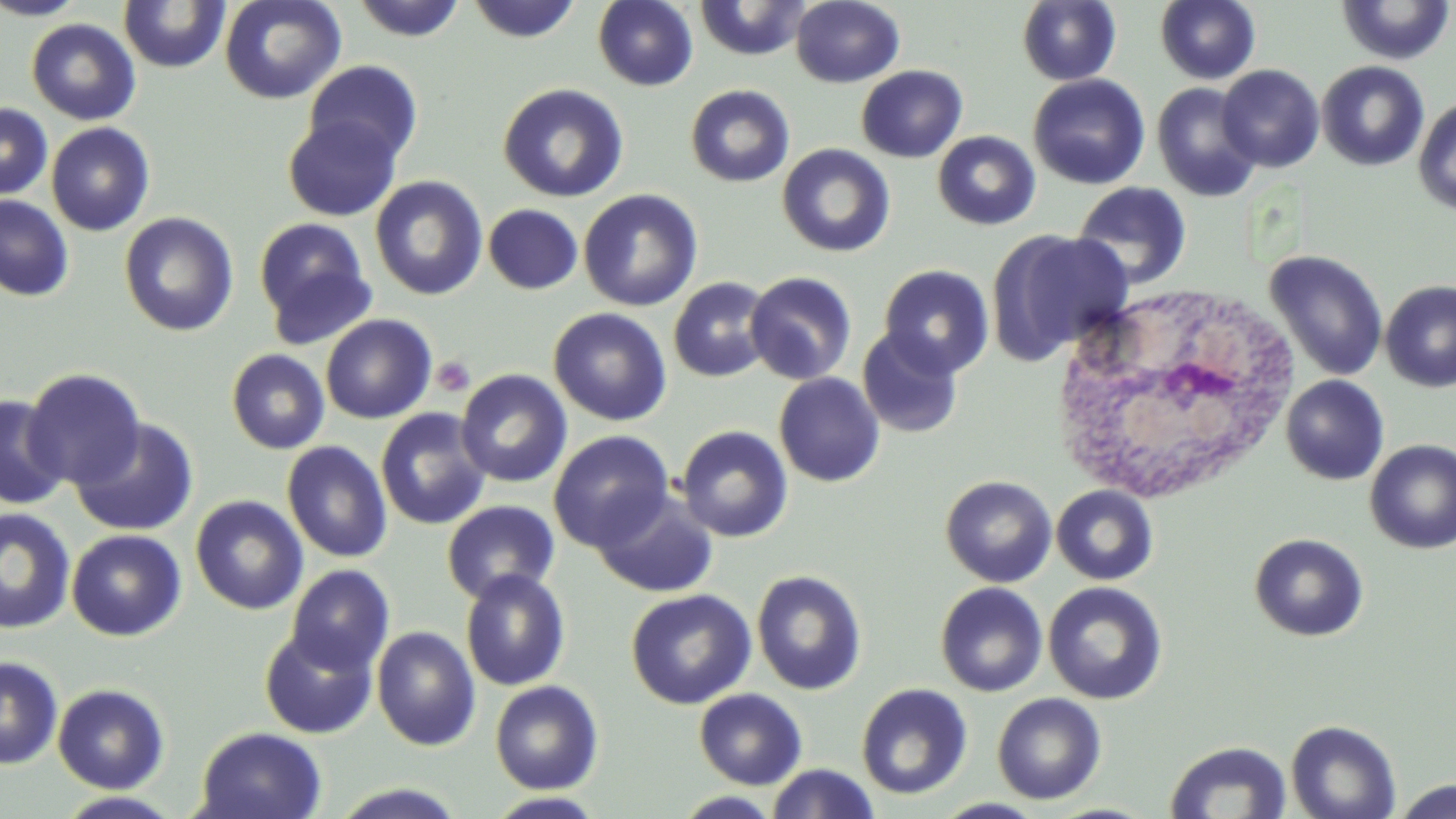
Summary:
  - Coordinate format: approximate bounding boxes as [x1, y1, x2, y2] in pixels
  - Platelet locations: [432, 355, 476, 397]
  - White blood cell locations: [1054, 290, 1305, 502]
  - Uninfected red blood cell locations: [0, 0, 91, 20], [218, 0, 346, 104], [349, 0, 469, 42], [465, 0, 583, 43], [692, 0, 814, 61], [791, 0, 905, 88], [1154, 0, 1261, 84], [1335, 0, 1456, 65], [118, 1, 230, 73], [592, 1, 698, 91], [1017, 1, 1121, 86], [26, 19, 141, 125], [303, 59, 423, 168], [1316, 61, 1429, 171], [1216, 64, 1325, 172], [856, 65, 968, 163], [1028, 74, 1150, 190], [498, 83, 629, 203], [1151, 83, 1262, 202], [685, 84, 795, 187], [1413, 97, 1456, 214], [0, 102, 52, 200], [283, 114, 402, 221], [45, 122, 155, 236], [932, 131, 1041, 230], [777, 143, 895, 257], [369, 176, 488, 301], [1071, 182, 1192, 290], [577, 189, 703, 311], [0, 194, 74, 302], [483, 204, 583, 294], [119, 212, 238, 336], [254, 217, 377, 342], [987, 229, 1133, 363], [1265, 250, 1388, 381], [878, 264, 994, 378], [744, 271, 858, 385], [668, 276, 774, 382], [1380, 280, 1456, 392], [548, 308, 672, 426], [320, 314, 437, 424], [856, 327, 964, 438], [226, 349, 330, 455], [429, 352, 477, 402], [22, 368, 146, 489], [455, 369, 573, 487], [773, 372, 885, 487], [1281, 375, 1389, 485], [0, 394, 70, 510], [375, 408, 492, 530], [70, 418, 199, 537], [676, 425, 793, 542], [548, 430, 675, 551], [1364, 440, 1456, 554], [281, 441, 392, 563], [940, 475, 1057, 587], [1051, 484, 1159, 585], [591, 490, 718, 598], [190, 495, 308, 615], [442, 500, 560, 604], [0, 507, 76, 634], [66, 529, 186, 642], [1248, 532, 1369, 642], [286, 564, 395, 675], [459, 568, 570, 691], [751, 568, 867, 695], [1043, 581, 1168, 705], [935, 582, 1048, 697], [626, 588, 756, 709], [259, 626, 378, 739], [371, 626, 481, 751], [0, 656, 63, 770], [489, 679, 604, 794], [855, 683, 973, 800], [52, 684, 170, 794], [694, 688, 807, 789], [992, 692, 1107, 805], [1285, 719, 1401, 819], [195, 727, 327, 819], [1163, 740, 1293, 818], [766, 763, 881, 819], [1391, 779, 1456, 819], [327, 783, 471, 819], [52, 791, 186, 818], [672, 791, 783, 818], [484, 792, 608, 818], [932, 798, 1048, 818]
  - Slide-level diagnosis: negative for blood parasites
  - Magnification: 1000x
  - Image size: 1456×819 pixels
  - Field of view: one of a larger specimen
  - Preparation: thin blood smear
  - Modality: light microscopy
  - Stain: May-Grünwald-Giemsa